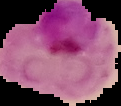

Summary:
  - Image type: segmented cell region on a black background
  - Image size: 121×106 pixels
  - Preparation: thin blood smear
  - Malaria status: parasitized